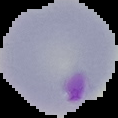

Summary:
  - Image size: 118×118 pixels
  - Image type: segmented cell region with the area outside set to black
  - Preparation: thin blood smear
  - Result: Plasmodium parasites identified